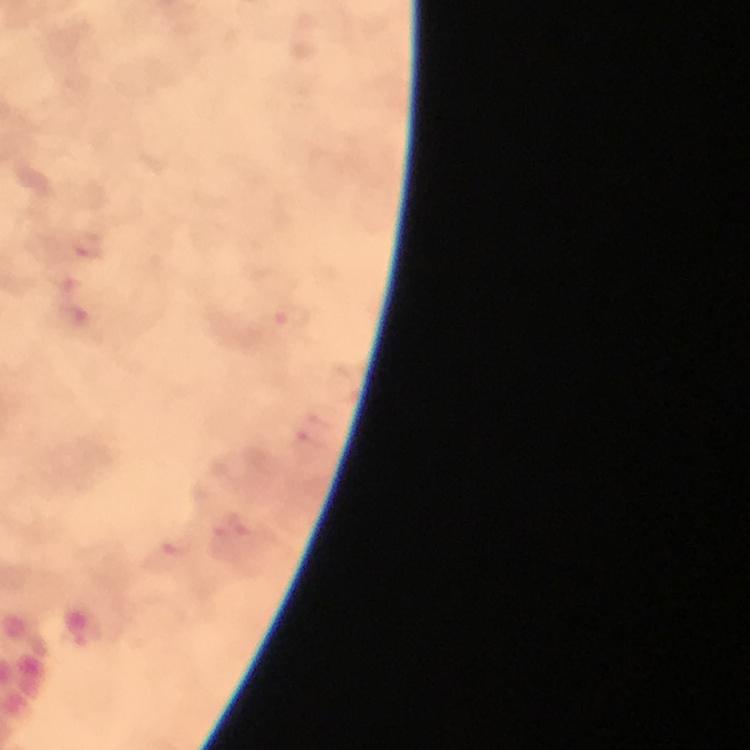
Approximate object centers, in pixels from the top-left corner.
Summary:
  - Plasmodium parasite locations: (x=88, y=244), (x=66, y=282), (x=74, y=315), (x=291, y=318), (x=316, y=412), (x=310, y=445), (x=231, y=528), (x=168, y=555)
  - Magnification: 100x
  - Preparation: thick smear
  - Context: from a diagnostic examination for malaria
  - Cropped from: a single field of view
  - Capture: smartphone camera through the microscope
  - Stain: Giemsa
  - Immersion oil: used
  - Image size: 750×750 pixels